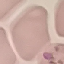
{
  "result": "no malaria parasites seen",
  "capture": "smartphone through the microscope eyepiece",
  "stain": "Giemsa",
  "image_type": "automatically extracted cell patch, resized to 64 × 64 pixels",
  "preparation": "thin blood film"
}